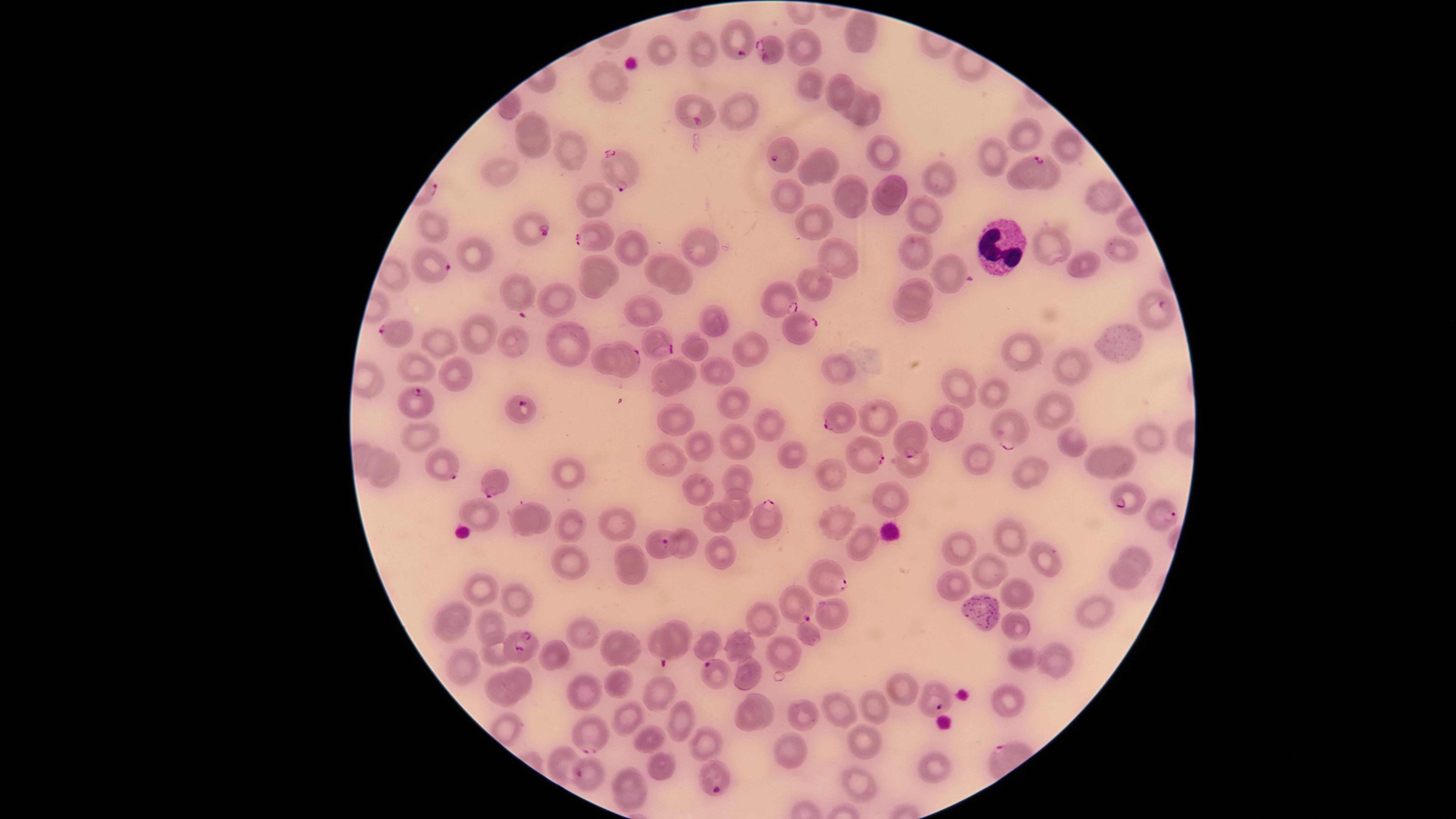
{
  "image_size": "1456×819 pixels",
  "stain": "Giemsa",
  "preparation": "thin smear of blood",
  "white_blood_cells": "approximate marker points as {x, y} in pixels: {997, 247}",
  "field_of_view": "single",
  "species": "Plasmodium falciparum",
  "visible_region": "circular",
  "uninfected_red_blood_cells": "approximate marker points as {x, y} in pixels: {862, 34}, {661, 45}, {704, 45}, {801, 48}, {611, 83}, {838, 84}, {805, 86}, {857, 96}, {865, 111}, {742, 113}, {532, 123}, {1022, 134}, {1066, 145}, {533, 149}, {571, 149}, {880, 152}, {825, 155}, {990, 160}, {502, 173}, {807, 175}, {928, 176}, {851, 180}, {898, 189}, {787, 196}, {596, 200}, {1105, 200}, {852, 202}, {883, 207}, {921, 211}, {818, 224}, {432, 225}, {632, 242}, {703, 244}, {1049, 246}, {918, 248}, {834, 250}, {1116, 252}, {479, 255}, {1080, 262}, {601, 263}, {652, 264}, {946, 275}, {684, 279}, {817, 281}, {593, 284}, {916, 288}, {516, 291}, {558, 299}, {644, 310}, {912, 314}, {712, 320}, {481, 333}, {567, 339}, {1121, 342}, {518, 343}, {445, 345}, {749, 346}, {695, 349}, {1019, 349}, {602, 357}, {690, 366}, {1069, 367}, {421, 368}, {836, 368}, {459, 372}, {715, 372}, {668, 381}, {955, 390}, {993, 394}, {731, 403}, {1054, 407}, {679, 416}, {877, 416}, {770, 422}, {415, 432}, {1149, 439}, {701, 443}, {739, 443}, {1075, 447}, {787, 451}, {975, 457}, {666, 458}, {370, 459}, {1127, 460}, {1101, 462}, {909, 466}, {567, 471}, {1025, 473}, {737, 476}, {833, 476}, {388, 478}, {693, 492}, {887, 498}, {740, 502}, {483, 514}, {545, 517}, {713, 517}, {521, 518}, {618, 522}, {839, 524}, {568, 528}, {1010, 540}, {960, 545}, {858, 547}, {681, 548}, {629, 552}, {722, 552}, {1138, 556}, {571, 560}, {1043, 563}, {986, 571}, {633, 576}, {1118, 579}, {950, 583}, {487, 592}, {515, 592}, {1021, 593}, {974, 603}, {455, 611}, {1097, 613}, {762, 619}, {824, 619}, {491, 624}, {1019, 627}, {677, 628}, {580, 632}, {450, 634}, {806, 636}, {609, 639}, {736, 644}, {707, 645}, {633, 648}, {494, 652}, {559, 654}, {776, 654}, {1021, 654}, {1058, 660}, {460, 666}, {522, 676}, {749, 677}, {620, 682}, {901, 686}, {503, 688}, {585, 689}, {653, 690}, {1005, 701}, {766, 703}, {877, 705}, {842, 714}, {805, 717}, {625, 718}, {746, 721}, {679, 723}, {649, 740}, {706, 742}, {863, 746}, {791, 756}, {564, 759}, {660, 769}, {933, 769}, {626, 779}, {858, 786}, {634, 801}",
  "capture": "smartphone photograph through the microscope eyepiece",
  "parasitized_red_blood_cells": "approximate marker points as {x, y} in pixels: {740, 37}, {769, 48}, {693, 110}, {784, 152}, {621, 167}, {1025, 170}, {527, 229}, {592, 236}, {434, 265}, {780, 296}, {1156, 315}, {801, 328}, {399, 335}, {657, 344}, {626, 361}, {414, 400}, {519, 405}, {834, 416}, {1006, 430}, {910, 441}, {866, 461}, {441, 465}, {494, 484}, {1125, 503}, {1161, 516}, {768, 522}, {660, 544}, {828, 579}, {795, 605}, {657, 645}, {518, 646}, {719, 677}, {929, 699}, {592, 737}, {587, 775}, {713, 779}",
  "presence": "malaria parasites identified"
}